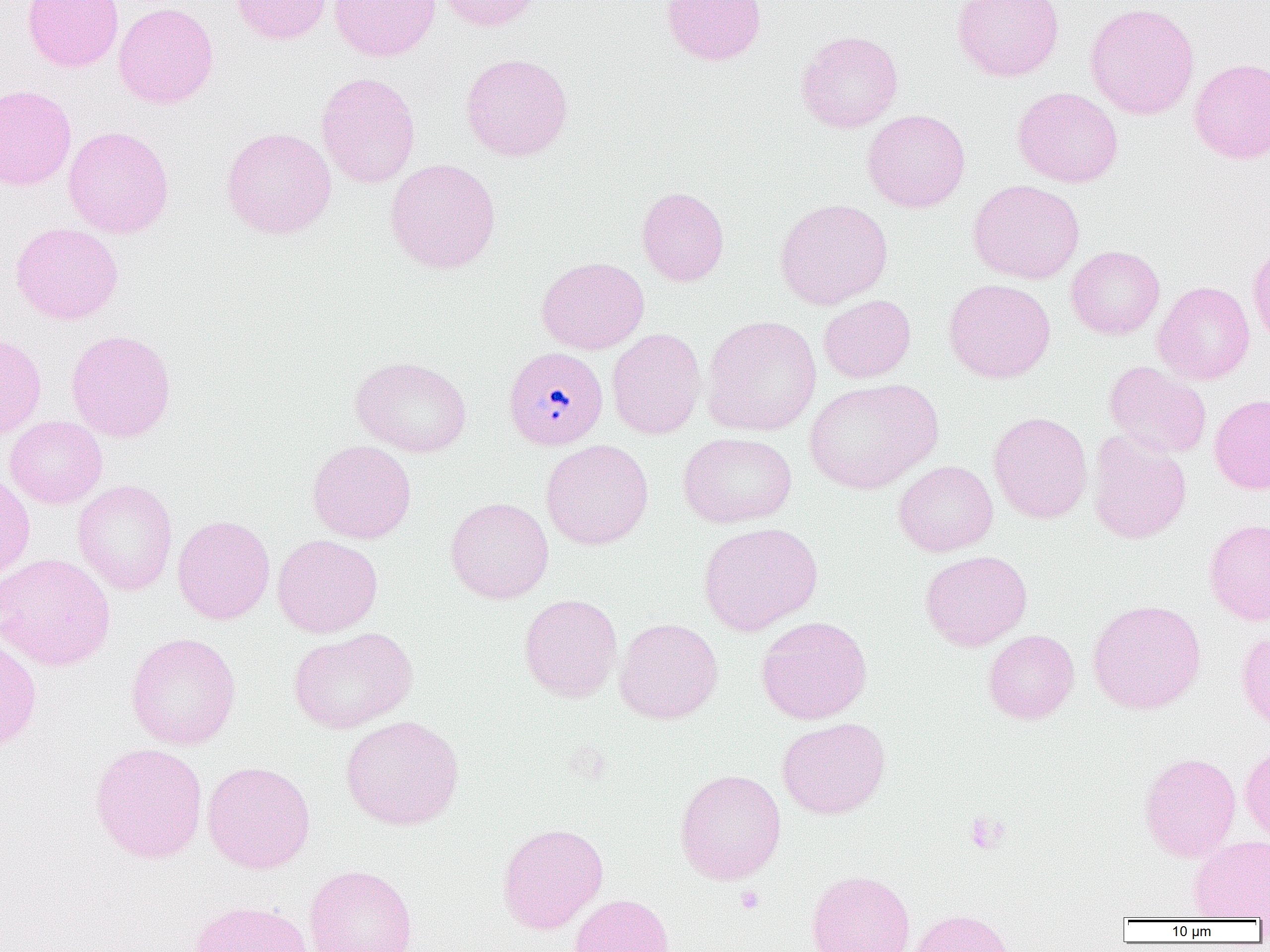
{
  "slide_level_diagnosis": "Plasmodium malariae",
  "magnification": "1000x",
  "modality": "optical microscopy",
  "uninfected_red_blood_cell_locations": "approximate bounding boxes as [x1, y1, x2, y2] in pixels: [22, 0, 123, 72], [232, 0, 332, 45], [329, 0, 440, 62], [436, 0, 545, 31], [661, 0, 767, 65], [952, 0, 1064, 81], [114, 2, 219, 109], [1085, 3, 1199, 120], [796, 30, 903, 133], [461, 53, 573, 161], [1189, 58, 1270, 163], [316, 72, 421, 188], [0, 84, 77, 191], [1012, 86, 1124, 188], [863, 109, 970, 212], [63, 126, 174, 238], [221, 127, 337, 239], [385, 158, 501, 274], [968, 179, 1085, 284], [637, 187, 729, 286], [774, 198, 893, 310], [10, 222, 123, 325], [1248, 243, 1270, 349], [1066, 246, 1165, 339], [537, 256, 649, 355], [944, 279, 1055, 383], [1153, 281, 1255, 385], [819, 295, 916, 383], [701, 316, 822, 436], [607, 328, 706, 440], [66, 329, 176, 442], [0, 333, 46, 440], [351, 355, 472, 458], [1104, 361, 1211, 459], [804, 378, 942, 495], [1209, 393, 1270, 494], [988, 412, 1092, 524], [5, 416, 107, 509], [1087, 429, 1191, 544], [678, 432, 797, 529], [541, 439, 654, 550], [307, 440, 416, 544], [893, 460, 998, 556], [0, 471, 35, 583], [73, 480, 178, 595], [445, 497, 554, 604], [173, 515, 275, 625], [1204, 518, 1270, 626], [698, 522, 823, 635], [272, 534, 383, 638], [920, 550, 1032, 651], [0, 552, 115, 672], [518, 593, 622, 702], [1087, 600, 1206, 714], [756, 615, 872, 724], [614, 617, 723, 724], [288, 627, 418, 734], [983, 629, 1079, 724], [1236, 629, 1270, 733], [126, 632, 241, 750], [0, 636, 42, 752], [340, 715, 464, 830], [777, 717, 890, 819], [89, 742, 208, 864], [1240, 743, 1270, 843], [1139, 752, 1241, 861], [202, 761, 315, 874], [674, 768, 787, 885], [497, 822, 608, 934], [1188, 834, 1270, 920], [304, 864, 418, 952], [806, 870, 915, 952], [570, 893, 675, 952], [187, 899, 314, 952], [907, 908, 1015, 952]",
  "image_size": "1270×952 pixels",
  "field_of_view": "single",
  "platelet_locations": "approximate bounding boxes as [x1, y1, x2, y2] in pixels: [965, 811, 1007, 854], [736, 886, 765, 913]",
  "preparation": "thin blood smear",
  "plasmodium_malariae_infected_red_blood_cell_locations": "approximate bounding boxes as [x1, y1, x2, y2] in pixels: [504, 347, 608, 449]"
}